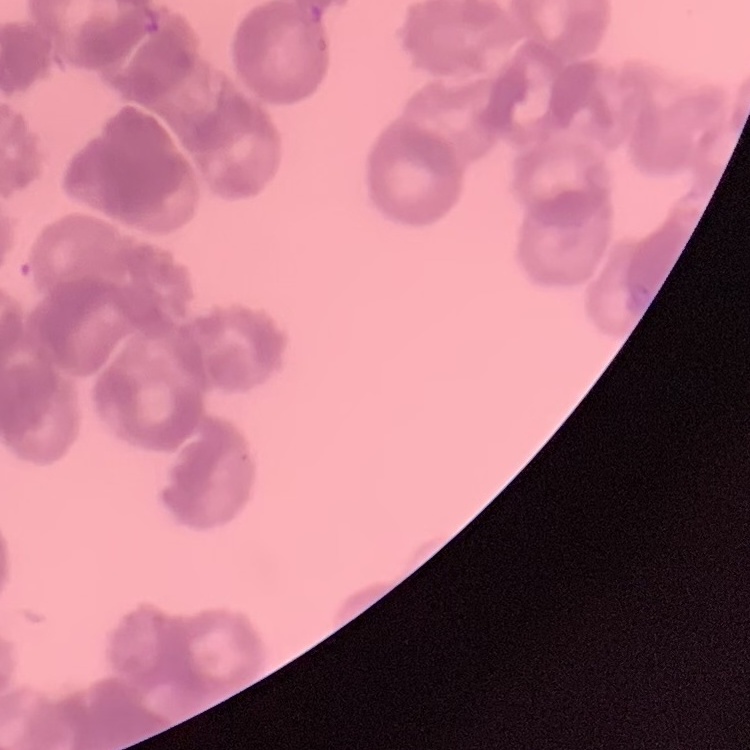
The erythrocytes exhibit rouleaux formation. Stained with either Field's or Giemsa. Thin peripheral smear. One tile cut from a larger photomicrograph.